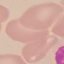

Summary:
  - Result: negative for malaria parasites
  - Preparation: thin blood smear
  - Stain: Giemsa
  - Capture: smartphone camera at the microscope eyepiece
  - Image type: automatically extracted cell patch, resized to 64 × 64 pixels